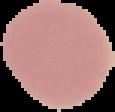
Summary:
  - Image type: segmented cell region with the area outside set to black
  - Image size: 115×112 pixels
  - Malaria status: uninfected
  - Preparation: thin blood smear